Give the position of every leukocyte visible.
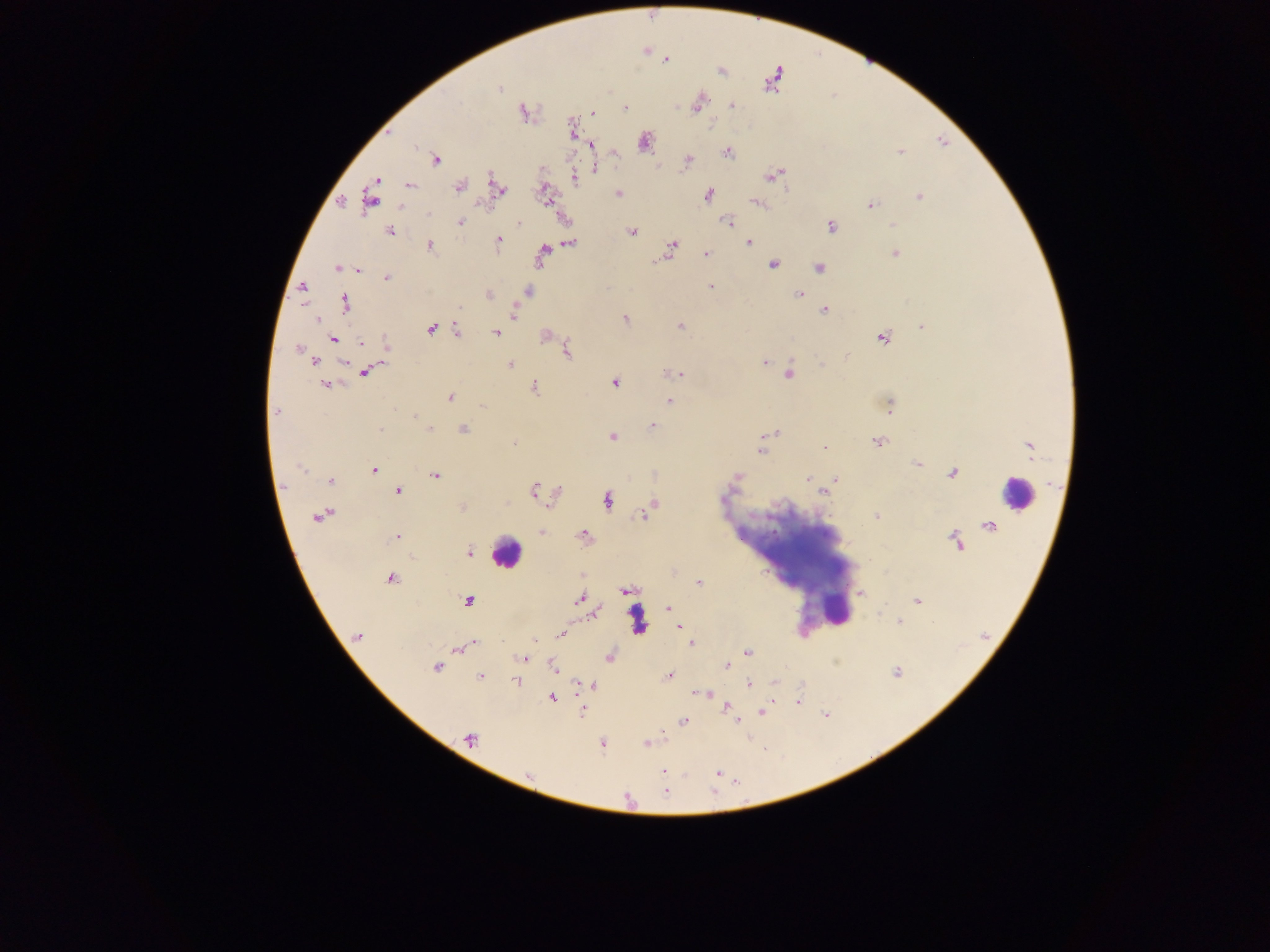

Approximate centers as {x, y} in pixels.
Leukocytes: {1011, 495}, {783, 550}, {507, 551}.

Plasmodium parasite locations: {767, 87}, {499, 90}, {699, 103}, {731, 106}, {625, 108}, {677, 108}, {696, 108}, {591, 112}, {522, 113}, {711, 121}, {643, 140}, {727, 153}, {436, 159}, {687, 160}, {685, 164}, {594, 170}, {770, 176}, {375, 180}, {409, 185}, {459, 187}, {501, 193}, {619, 193}, {709, 194}, {754, 202}, {869, 204}, {399, 205}, {728, 220}, {461, 221}, {520, 225}, {831, 225}, {391, 231}, {632, 232}, {498, 240}, {750, 243}, {431, 245}, {673, 248}, {706, 254}, {772, 264}, {818, 266}, {337, 267}, {359, 270}, {387, 277}, {710, 286}, {489, 294}, {798, 295}, {305, 306}, {459, 307}, {824, 310}, {513, 313}, {625, 318}, {319, 320}, {679, 325}, {922, 327}, {456, 328}, {495, 332}, {546, 336}, {881, 339}, {361, 343}, {567, 344}, {298, 350}, {567, 351}, {847, 356}, {766, 361}, {821, 361}, {342, 362}, {511, 363}, {376, 367}, {665, 372}, {364, 374}, {681, 374}, {326, 385}, {535, 385}, {614, 385}, {450, 397}, {670, 400}, {482, 406}, {891, 409}, {276, 410}, {415, 416}, {653, 426}, {431, 428}, {464, 428}, {381, 430}, {775, 431}, {611, 437}, {513, 441}, {878, 441}, {762, 442}, {824, 448}, {1028, 450}, {915, 465}, {302, 469}, {374, 469}, {435, 475}, {656, 476}, {806, 479}, {835, 479}, {331, 480}, {534, 489}, {399, 490}, {558, 490}, {821, 491}, {655, 503}, {550, 504}, {316, 517}, {876, 518}, {542, 533}, {584, 533}, {399, 536}, {950, 536}, {394, 538}, {470, 552}, {390, 578}, {699, 583}, {859, 593}, {579, 597}, {916, 600}, {669, 607}, {595, 615}, {901, 622}, {677, 627}, {559, 633}, {357, 637}, {534, 639}, {692, 646}, {456, 650}, {746, 652}, {525, 659}, {554, 666}, {437, 667}, {725, 667}, {669, 676}, {480, 678}, {515, 682}, {748, 684}, {594, 686}, {696, 694}, {710, 694}, {552, 696}, {712, 698}, {726, 707}, {582, 712}, {760, 712}, {733, 716}, {683, 721}, {736, 722}, {468, 740}, {602, 743}, {645, 743}, {661, 772}, {718, 774}, {665, 792}. Single field of view. Thick blood film. Mobile-phone photograph taken through the microscope. Collected in Ghana. Image is 1270×952 pixels.